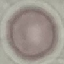
Summary:
  - Result: no malaria parasites seen
  - Preparation: thin blood smear
  - Capture: smartphone through the microscope eyepiece
  - Stain: Giemsa
  - Image type: automatically extracted cell patch, resized to 64 × 64 pixels